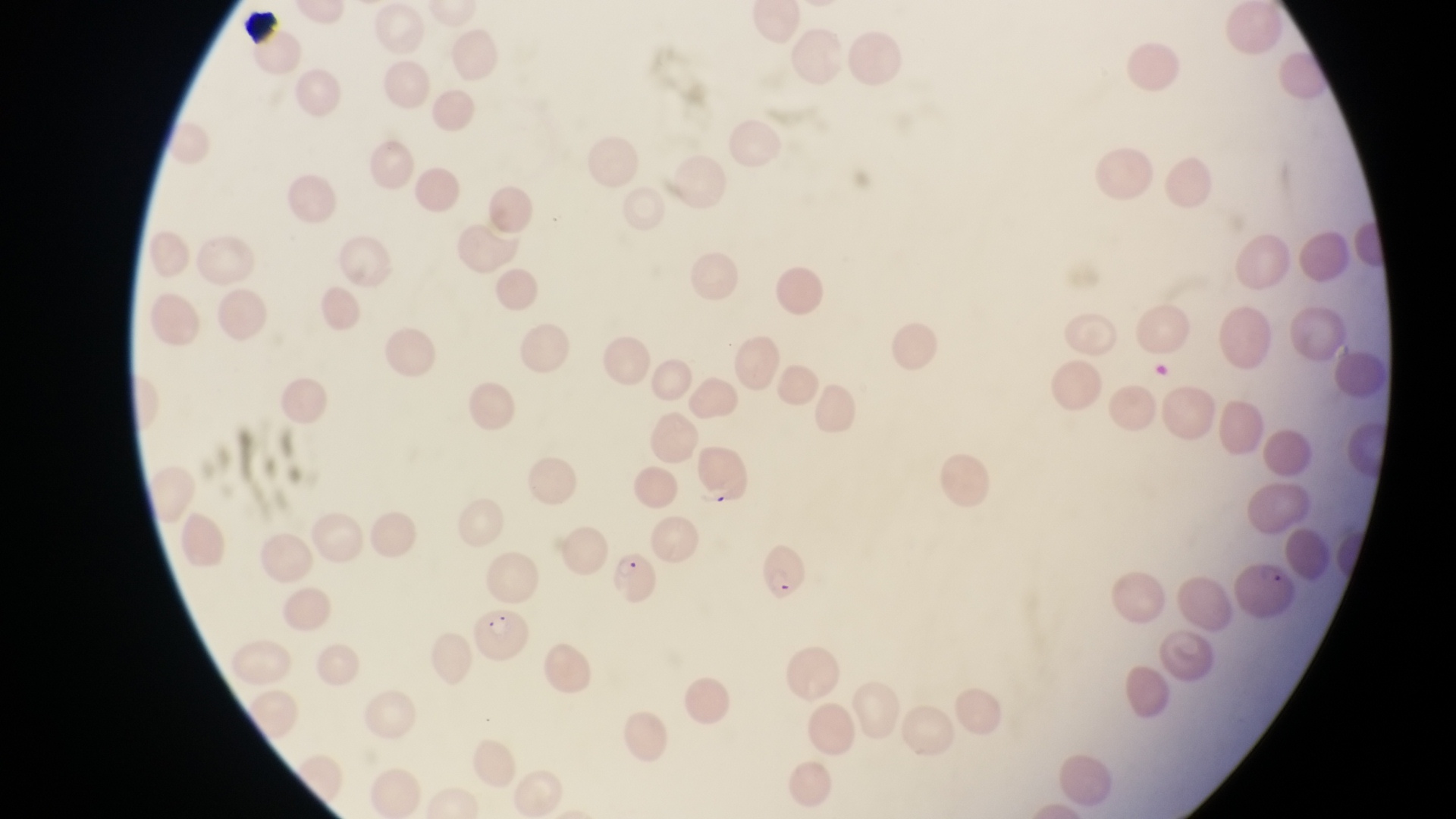

capture = smartphone photograph through the eyepiece of an Olympus CX-23 microscope
country = Uganda
parasitised red blood cell locations = approximate bounding boxes as left top right bottom in pixels: 695 452 756 512; 758 541 813 610; 608 544 658 607; 1234 554 1298 626; 472 610 530 671
preparation = thin blood smear
image size = 1456×819 pixels
field of view = single
magnification = 1000x